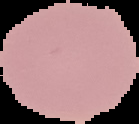

preparation = thin blood film
result = no Plasmodium parasites seen
image size = 139×124 pixels
image type = cell region segmented out of the field of view; surrounding area masked to black